Name the parasite shown.
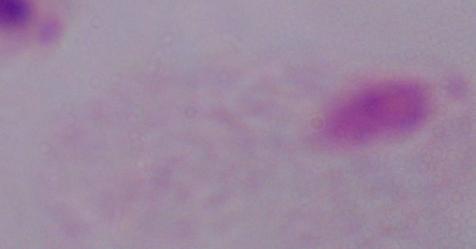
This is a trichomonad.

Captured at 1000x magnification. Photomicrograph.